State which parasite is depicted.
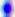
This is Toxoplasma gondii.

Micrograph. Captured at 400x magnification.